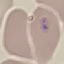

Summary:
  - Result: no malaria parasites detected
  - Capture: smartphone camera at the microscope eyepiece
  - Image type: automatically extracted cell patch, resized to 64 × 64 pixels
  - Preparation: thin blood smear
  - Stain: Giemsa